State which parasite is depicted.
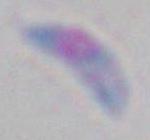

Toxoplasma gondii.

Summary:
  - Magnification: 1000x
  - Modality: micrograph